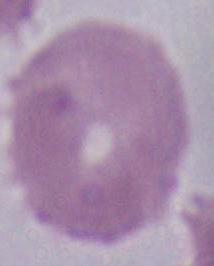
Summary:
  - Magnification: 1000x
  - Modality: photomicrograph
  - Identification: erythrocyte